Identify the blood parasite species.
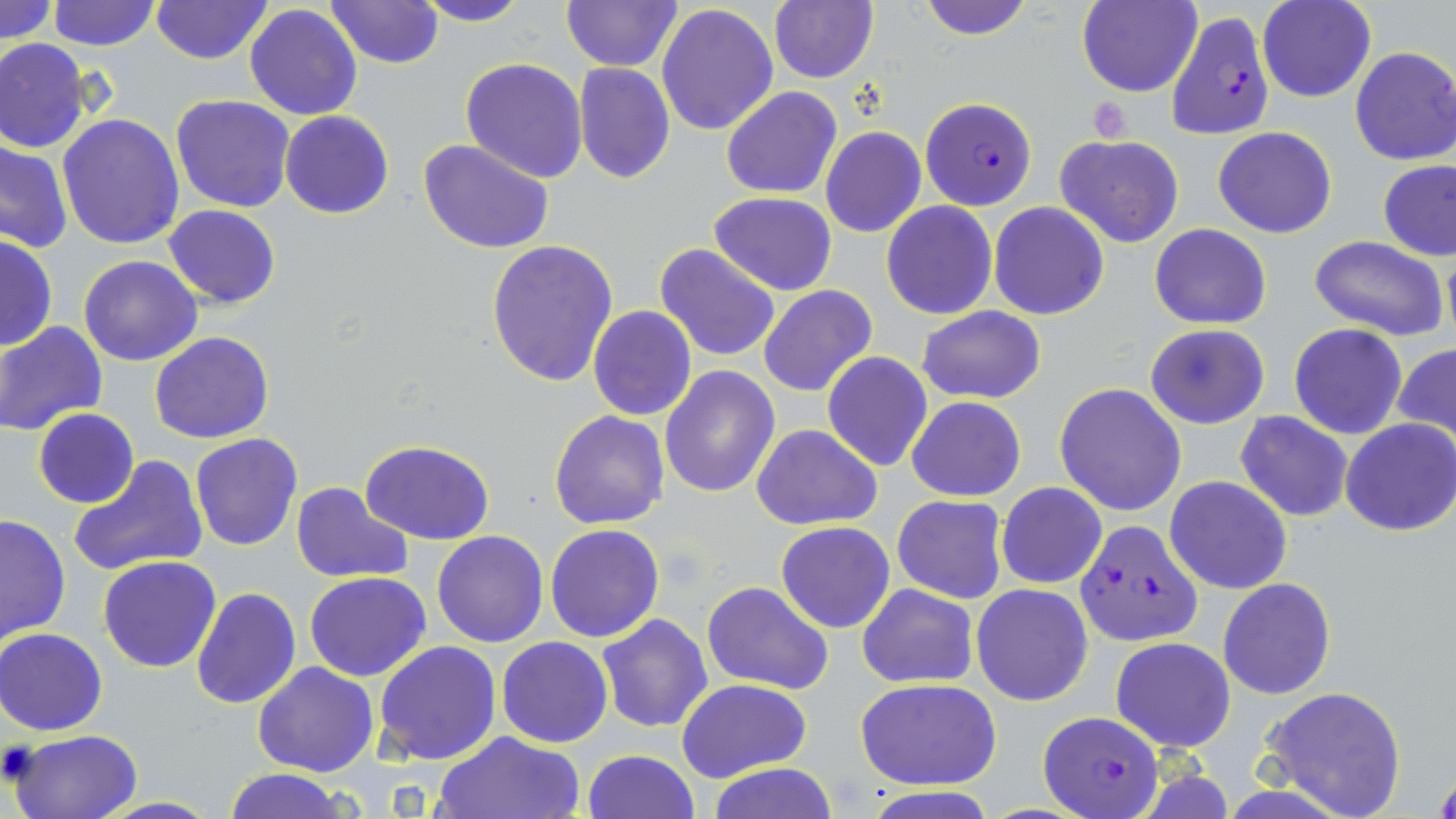

Plasmodium falciparum.

Summary:
  - Coordinate format: approximate bounding boxes as named x1/y1/x2/y2 corners in pixels
  - Plasmodium falciparum-infected red blood cell locations: (x1=1167, y1=9, x2=1274, y2=140), (x1=921, y1=96, x2=1037, y2=210), (x1=1072, y1=519, x2=1201, y2=646), (x1=1038, y1=712, x2=1160, y2=817)
  - Uninfected red blood cell locations: (x1=1, y1=0, x2=58, y2=45), (x1=47, y1=0, x2=160, y2=51), (x1=324, y1=0, x2=444, y2=68), (x1=414, y1=0, x2=534, y2=26), (x1=916, y1=0, x2=1035, y2=39), (x1=1077, y1=0, x2=1201, y2=98), (x1=1258, y1=0, x2=1375, y2=102), (x1=150, y1=1, x2=272, y2=65), (x1=560, y1=1, x2=681, y2=71), (x1=769, y1=1, x2=877, y2=84), (x1=244, y1=4, x2=362, y2=120), (x1=656, y1=4, x2=778, y2=136), (x1=0, y1=38, x2=90, y2=153), (x1=1349, y1=46, x2=1456, y2=166), (x1=460, y1=57, x2=588, y2=182), (x1=573, y1=63, x2=675, y2=184), (x1=721, y1=86, x2=842, y2=198), (x1=169, y1=94, x2=295, y2=213), (x1=279, y1=110, x2=394, y2=220), (x1=56, y1=114, x2=185, y2=250), (x1=821, y1=126, x2=927, y2=239), (x1=1214, y1=127, x2=1337, y2=238), (x1=1055, y1=134, x2=1184, y2=247), (x1=419, y1=139, x2=554, y2=254), (x1=0, y1=140, x2=73, y2=253), (x1=1377, y1=159, x2=1456, y2=261), (x1=709, y1=192, x2=837, y2=294), (x1=883, y1=202, x2=997, y2=320), (x1=990, y1=203, x2=1109, y2=320), (x1=164, y1=204, x2=280, y2=308), (x1=1149, y1=225, x2=1272, y2=328), (x1=0, y1=233, x2=57, y2=352), (x1=1307, y1=235, x2=1451, y2=341), (x1=485, y1=239, x2=619, y2=386), (x1=654, y1=243, x2=781, y2=361), (x1=78, y1=255, x2=202, y2=367), (x1=27, y1=270, x2=152, y2=396), (x1=759, y1=285, x2=878, y2=396), (x1=587, y1=305, x2=697, y2=421), (x1=917, y1=305, x2=1046, y2=405), (x1=1, y1=320, x2=107, y2=436), (x1=1145, y1=323, x2=1270, y2=429), (x1=1289, y1=323, x2=1407, y2=439), (x1=149, y1=332, x2=275, y2=443), (x1=1392, y1=341, x2=1456, y2=454), (x1=822, y1=352, x2=933, y2=472), (x1=660, y1=367, x2=780, y2=499), (x1=1054, y1=382, x2=1187, y2=517), (x1=906, y1=396, x2=1025, y2=501), (x1=33, y1=409, x2=139, y2=509), (x1=550, y1=410, x2=670, y2=529), (x1=1235, y1=410, x2=1354, y2=523), (x1=1340, y1=419, x2=1456, y2=536), (x1=752, y1=424, x2=880, y2=530), (x1=190, y1=433, x2=303, y2=550), (x1=359, y1=439, x2=495, y2=545), (x1=67, y1=456, x2=208, y2=577), (x1=1165, y1=476, x2=1292, y2=593), (x1=292, y1=482, x2=412, y2=582), (x1=996, y1=483, x2=1106, y2=589), (x1=892, y1=494, x2=1008, y2=604), (x1=0, y1=512, x2=72, y2=646), (x1=775, y1=521, x2=896, y2=633), (x1=545, y1=523, x2=665, y2=642), (x1=430, y1=531, x2=548, y2=647), (x1=97, y1=556, x2=222, y2=673), (x1=303, y1=572, x2=431, y2=681), (x1=1217, y1=576, x2=1336, y2=700), (x1=703, y1=582, x2=835, y2=694), (x1=856, y1=582, x2=979, y2=689), (x1=972, y1=583, x2=1093, y2=707), (x1=191, y1=587, x2=301, y2=710), (x1=597, y1=613, x2=713, y2=732), (x1=0, y1=627, x2=108, y2=736), (x1=498, y1=636, x2=613, y2=747), (x1=1109, y1=636, x2=1236, y2=752), (x1=373, y1=641, x2=503, y2=766), (x1=252, y1=661, x2=379, y2=777), (x1=854, y1=678, x2=1002, y2=790), (x1=678, y1=679, x2=811, y2=783), (x1=1259, y1=687, x2=1407, y2=818), (x1=8, y1=728, x2=142, y2=819), (x1=431, y1=731, x2=585, y2=819), (x1=582, y1=749, x2=700, y2=819), (x1=704, y1=762, x2=841, y2=818), (x1=222, y1=768, x2=350, y2=819)
  - Platelet locations: (x1=1090, y1=96, x2=1136, y2=142)
  - Image size: 1456×819 pixels
  - Magnification: 1000x
  - Stain: May-Grünwald-Giemsa
  - Field of view: single
  - Preparation: thin blood film
  - Modality: optical microscopy